State the preparation type.
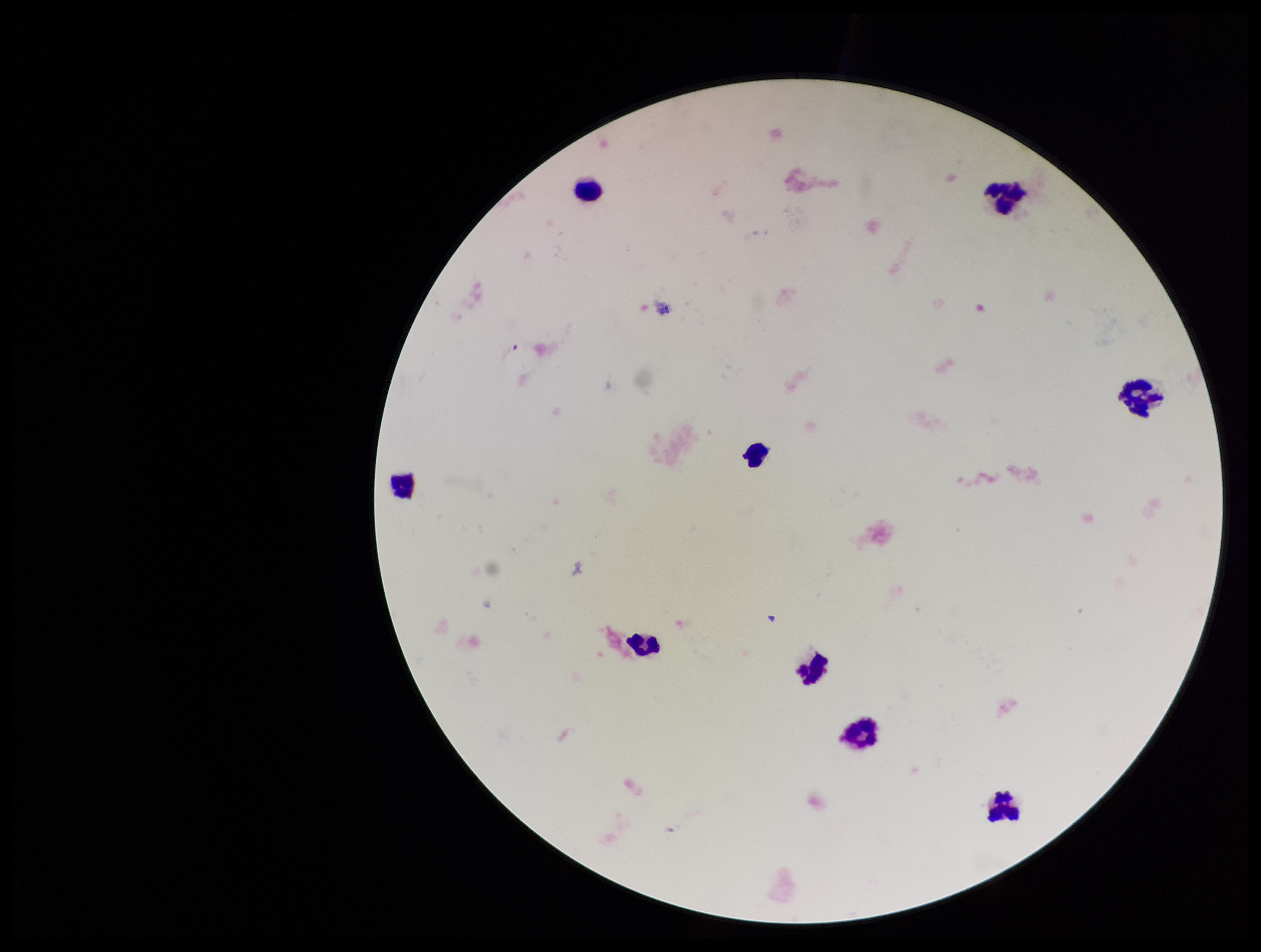
A thick smear.

parasite count = 0
Plasmodium parasites = none identified
field of view = one from this slide
capture = smartphone photograph through the microscope eyepiece
leukocyte count = 9
image size = 1261×952 pixels
patient malaria status = negative
stain = Giemsa